State the blood parasite species.
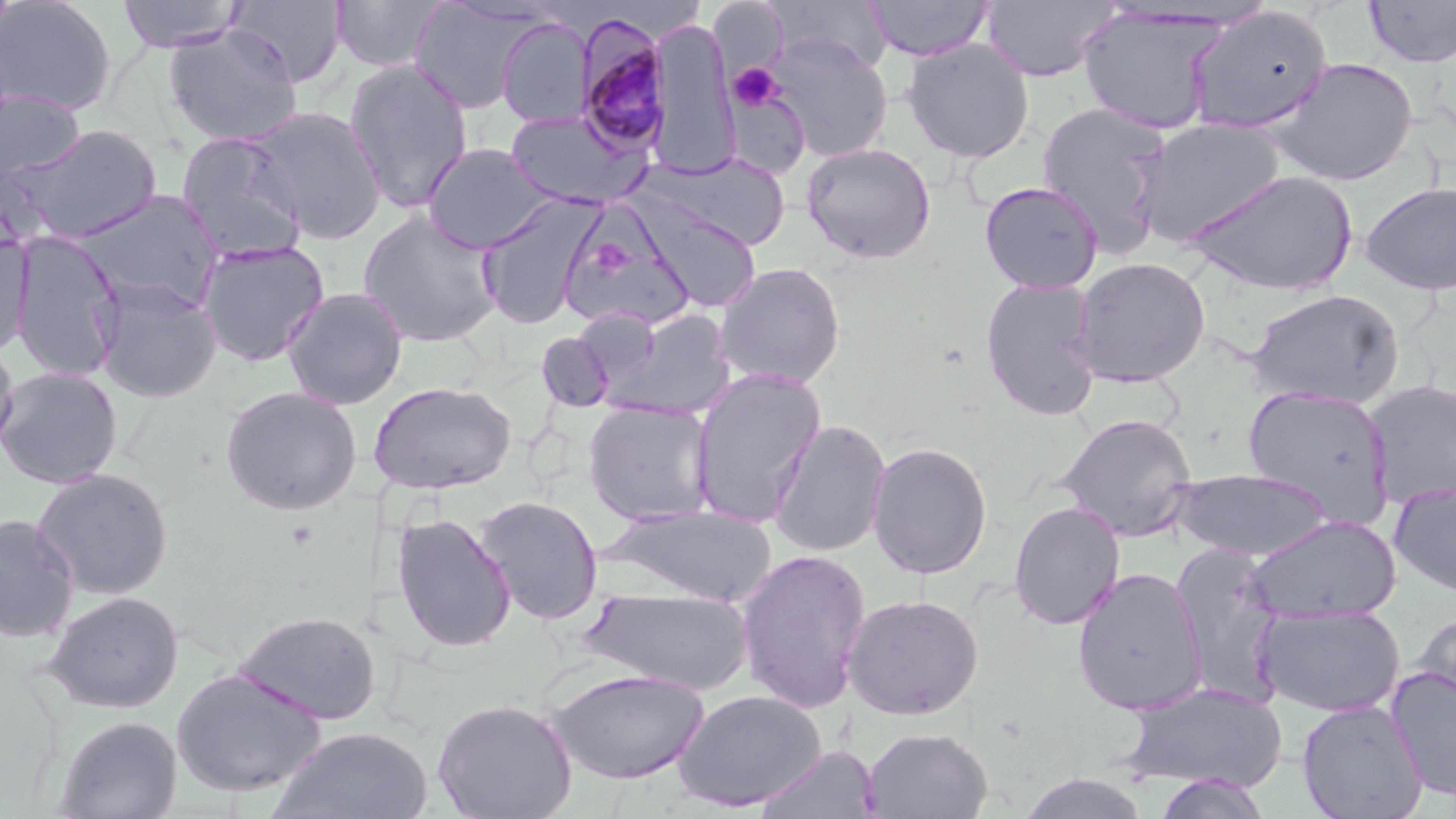

Plasmodium malariae.

Approximate bounding boxes as named x1/y1/x2/y2 corners in pixels. Uninfected red blood cell locations: (x1=0, y1=0, x2=116, y2=116), (x1=116, y1=0, x2=246, y2=53), (x1=227, y1=0, x2=348, y2=87), (x1=329, y1=0, x2=446, y2=72), (x1=864, y1=0, x2=993, y2=61), (x1=409, y1=1, x2=537, y2=114), (x1=709, y1=1, x2=789, y2=80), (x1=770, y1=1, x2=893, y2=75), (x1=980, y1=1, x2=1118, y2=82), (x1=1363, y1=1, x2=1456, y2=68), (x1=1184, y1=5, x2=1334, y2=135), (x1=1077, y1=7, x2=1224, y2=135), (x1=646, y1=16, x2=740, y2=178), (x1=496, y1=18, x2=593, y2=127), (x1=163, y1=27, x2=303, y2=146), (x1=763, y1=32, x2=893, y2=161), (x1=902, y1=39, x2=1034, y2=163), (x1=1268, y1=57, x2=1420, y2=186), (x1=343, y1=59, x2=474, y2=214), (x1=0, y1=90, x2=85, y2=183), (x1=1036, y1=101, x2=1174, y2=254), (x1=246, y1=105, x2=386, y2=244), (x1=505, y1=109, x2=649, y2=209), (x1=1132, y1=117, x2=1287, y2=245), (x1=5, y1=123, x2=163, y2=243), (x1=175, y1=131, x2=308, y2=262), (x1=801, y1=142, x2=937, y2=263), (x1=423, y1=143, x2=556, y2=253), (x1=645, y1=152, x2=792, y2=251), (x1=1184, y1=168, x2=1359, y2=296), (x1=979, y1=180, x2=1104, y2=294), (x1=1359, y1=180, x2=1456, y2=296), (x1=73, y1=190, x2=224, y2=313), (x1=477, y1=194, x2=603, y2=330), (x1=638, y1=199, x2=761, y2=311), (x1=358, y1=209, x2=503, y2=347), (x1=559, y1=218, x2=696, y2=333), (x1=10, y1=230, x2=125, y2=382), (x1=0, y1=233, x2=34, y2=355), (x1=196, y1=239, x2=330, y2=367), (x1=1071, y1=256, x2=1211, y2=387), (x1=714, y1=261, x2=847, y2=388), (x1=979, y1=276, x2=1103, y2=421), (x1=95, y1=277, x2=222, y2=403), (x1=281, y1=287, x2=408, y2=410), (x1=1245, y1=289, x2=1404, y2=409), (x1=602, y1=309, x2=737, y2=420), (x1=536, y1=332, x2=615, y2=412), (x1=0, y1=337, x2=20, y2=459), (x1=0, y1=367, x2=123, y2=489), (x1=689, y1=368, x2=826, y2=527), (x1=1362, y1=379, x2=1456, y2=509), (x1=369, y1=381, x2=516, y2=494), (x1=1242, y1=385, x2=1396, y2=525), (x1=220, y1=386, x2=362, y2=515), (x1=582, y1=400, x2=717, y2=526), (x1=1057, y1=413, x2=1198, y2=541), (x1=767, y1=418, x2=891, y2=558), (x1=866, y1=441, x2=994, y2=579), (x1=32, y1=468, x2=174, y2=600), (x1=1170, y1=468, x2=1333, y2=561), (x1=1388, y1=480, x2=1456, y2=596), (x1=473, y1=495, x2=604, y2=624), (x1=1008, y1=500, x2=1126, y2=630), (x1=607, y1=504, x2=777, y2=605), (x1=391, y1=512, x2=516, y2=653), (x1=1, y1=514, x2=79, y2=642), (x1=1245, y1=514, x2=1402, y2=624), (x1=1168, y1=544, x2=1288, y2=706), (x1=735, y1=548, x2=872, y2=714), (x1=1072, y1=568, x2=1208, y2=715), (x1=582, y1=586, x2=756, y2=693), (x1=44, y1=589, x2=184, y2=713), (x1=842, y1=593, x2=984, y2=721), (x1=1255, y1=604, x2=1405, y2=717), (x1=234, y1=609, x2=381, y2=725), (x1=1412, y1=610, x2=1456, y2=721), (x1=1386, y1=666, x2=1456, y2=800), (x1=171, y1=667, x2=327, y2=798), (x1=547, y1=668, x2=711, y2=784), (x1=1119, y1=681, x2=1287, y2=793), (x1=671, y1=689, x2=827, y2=811), (x1=432, y1=697, x2=577, y2=819), (x1=1297, y1=698, x2=1428, y2=819), (x1=55, y1=715, x2=182, y2=819), (x1=270, y1=726, x2=434, y2=818), (x1=862, y1=726, x2=994, y2=819), (x1=753, y1=745, x2=881, y2=819), (x1=1016, y1=771, x2=1153, y2=818), (x1=1153, y1=774, x2=1273, y2=819). Platelet locations: (x1=727, y1=63, x2=782, y2=111). Plasmodium malariae-infected red blood cell locations: (x1=574, y1=19, x2=672, y2=156). Thin blood smear. Captured at 1000x magnification. Image is 1456×819 pixels. Optical microscopy. May-Grünwald-Giemsa stain. One field of a larger specimen.